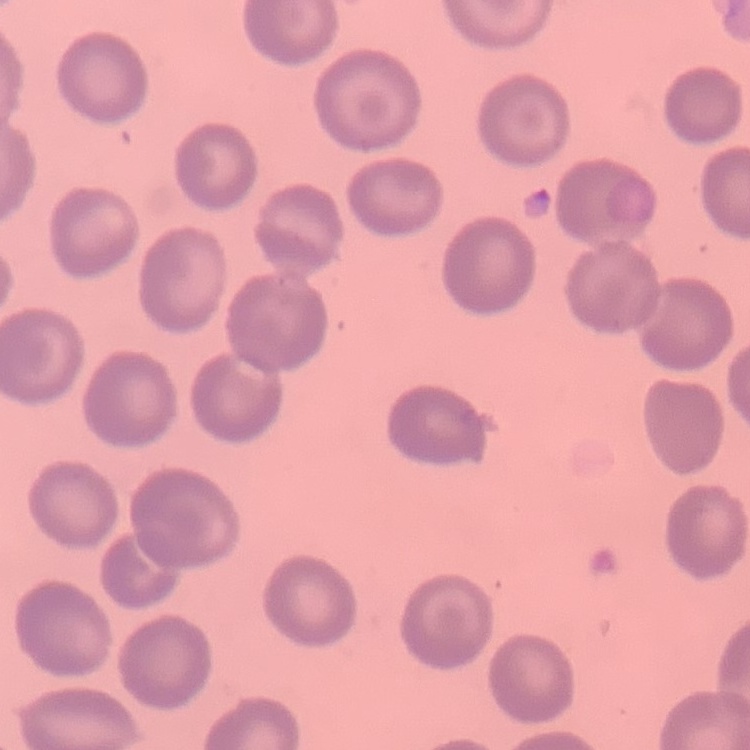
The red blood cells show no rouleaux formation. Thin blood film. Square crop of a larger photomicrograph. Stained with either Field's or Giemsa.